Classify this cell by malaria status.
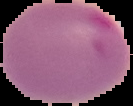
Parasitized.

Summary:
  - Image size: 133×106 pixels
  - Image type: segmented cell region on a black background
  - Preparation: thin blood smear